Comment on the morphology of the red blood cells.
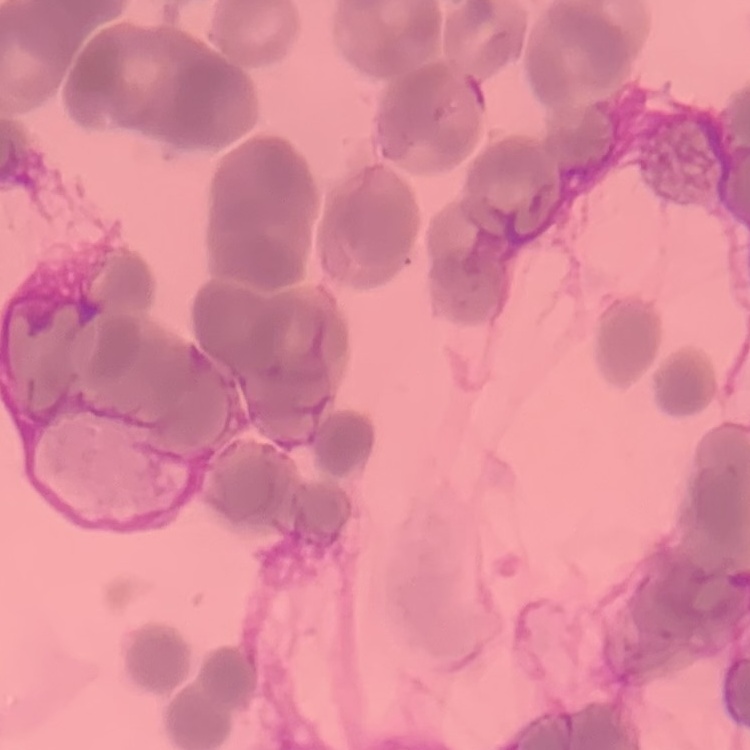
They show rouleaux formation.

Summary:
  - Preparation: thin blood film
  - Stain: Field's or Giemsa
  - Image type: one tile cut from a larger photomicrograph